Name the parasite shown.
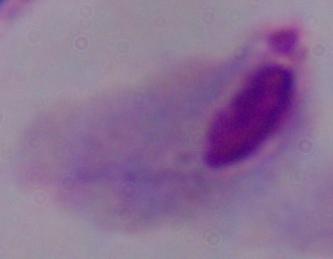
This is a trichomonad.

Summary:
  - Magnification: 1000x
  - Modality: photomicrograph